Assess for malaria.
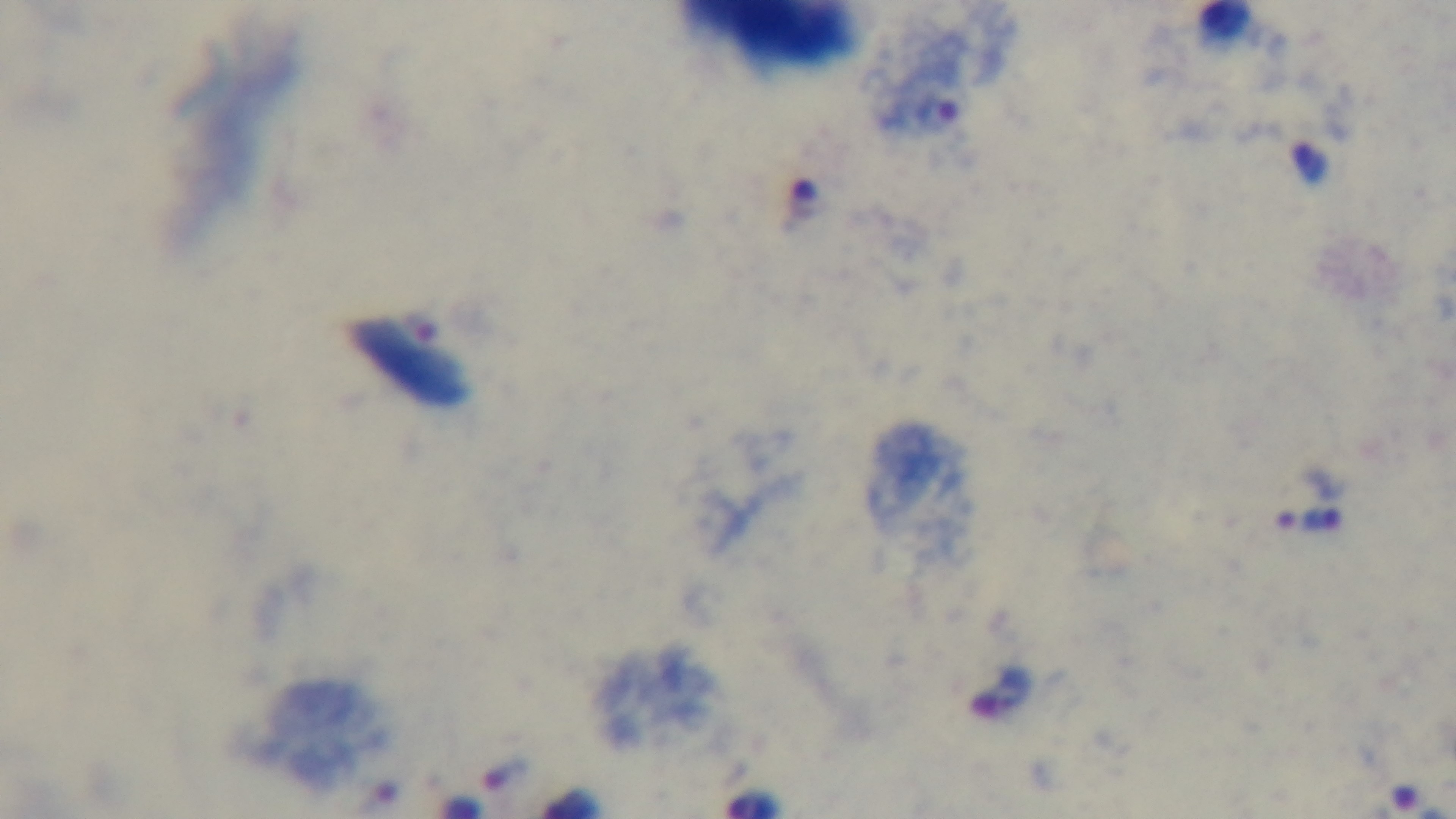
Infected.

{
  "stain": "Giemsa",
  "modality": "light microscopy",
  "preparation": "thick blood film",
  "field_of_view": "single",
  "objective": "100x oil immersion",
  "capture": "mounted 4K digital camera"
}